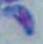

modality: micrograph
identification: Toxoplasma gondii
magnification: 1000x